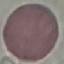
{
  "malaria_status": "uninfected",
  "capture": "smartphone camera at the microscope eyepiece",
  "preparation": "thin blood film",
  "image_type": "cell patch, automatically extracted from a larger field of view and resized to 64 × 64 pixels",
  "stain": "Giemsa"
}